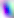
Summary:
  - Modality: photomicrograph
  - Identification: Toxoplasma gondii
  - Magnification: 400x